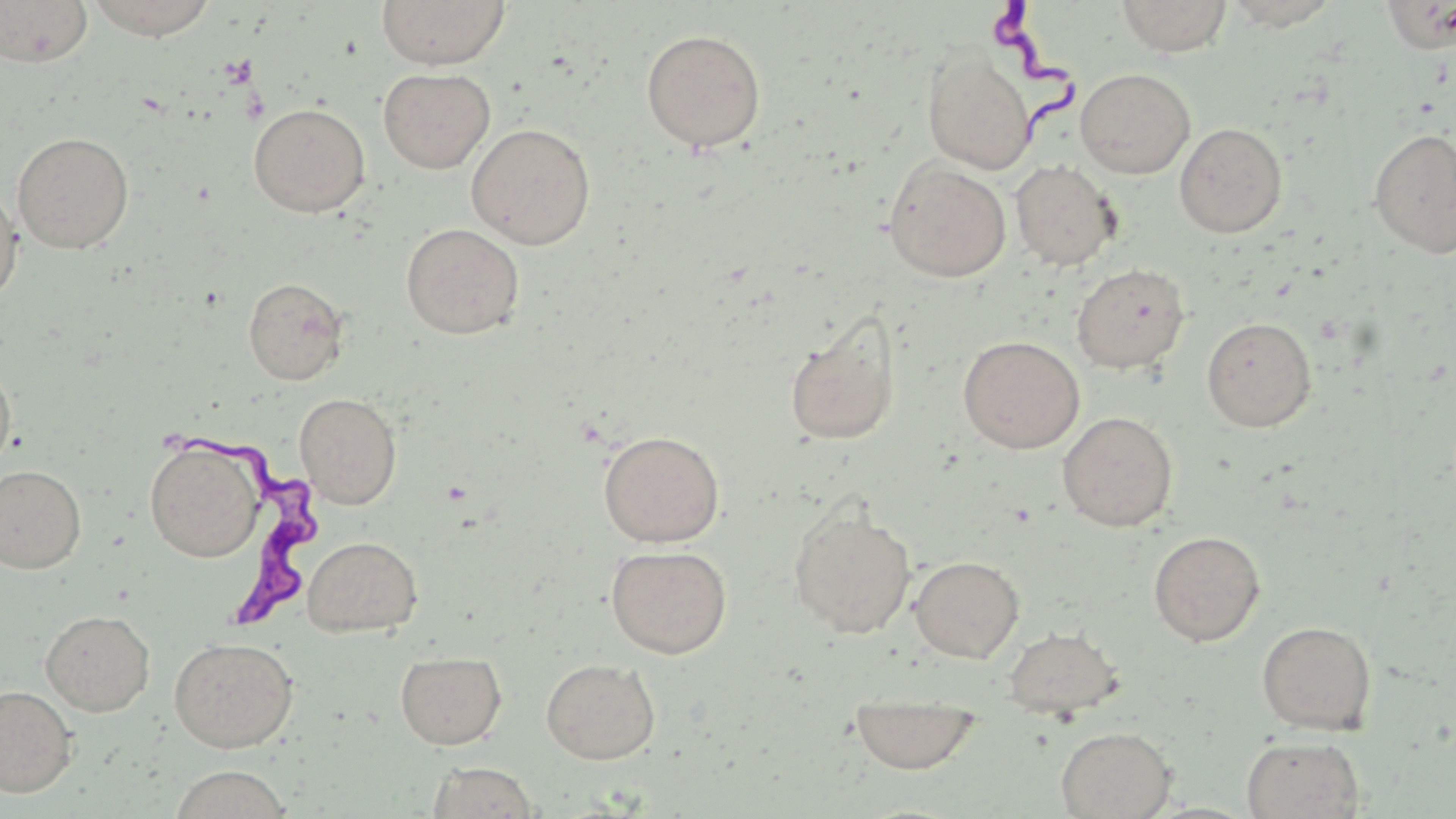 Approximate bounding boxes as (x1,y1)-(x2,y2) corner pairs in pixels. Trypanosoma brucei locations: (984,0)-(1075,136), (182,430)-(320,627). Uninfected red blood cell locations: (0,0)-(93,67), (84,0)-(219,39), (376,0)-(510,69), (1116,0)-(1234,57), (1218,1)-(1344,30), (641,28)-(766,152), (922,51)-(1035,174), (378,68)-(495,174), (1075,68)-(1196,179), (248,103)-(370,217), (465,123)-(596,249), (1174,123)-(1288,238), (1369,128)-(1456,259), (12,132)-(134,253), (883,159)-(1011,283), (1010,160)-(1120,271), (0,183)-(23,308), (401,223)-(525,339), (1071,263)-(1190,374), (242,277)-(349,385), (783,314)-(902,447), (1201,316)-(1317,432), (958,335)-(1085,454), (0,355)-(16,475), (295,392)-(402,509), (1057,411)-(1178,531), (598,429)-(725,547), (145,438)-(264,562), (0,464)-(86,574), (788,504)-(917,638), (1148,530)-(1266,646), (302,535)-(423,637), (605,544)-(733,658), (910,555)-(1024,663), (41,609)-(155,716), (1256,620)-(1377,735), (1003,625)-(1125,719), (168,636)-(298,752), (395,650)-(507,749), (541,658)-(661,764), (0,685)-(78,797), (848,690)-(982,774), (1056,726)-(1176,818), (1241,735)-(1365,819), (425,761)-(541,818), (168,766)-(294,819). Slide-level diagnosis: Trypanosoma brucei. Thin blood smear. Single field of view. Optical microscopy. Image is 1456×819 pixels. May-Grünwald-Giemsa stain. Captured at 1000x magnification.